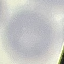
malaria_status: uninfected
capture: smartphone through the microscope eyepiece
image_type: cell patch, automatically extracted from a larger field of view and resized to 64 × 64 pixels
stain: Giemsa
preparation: thin blood smear